Assess this cell for malaria.
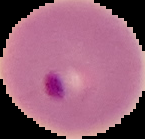

It is parasitized.

Summary:
  - Image size: 145×139 pixels
  - Preparation: thin blood smear
  - Image type: segmented cell region with the area outside set to black